Locate every malaria parasite.
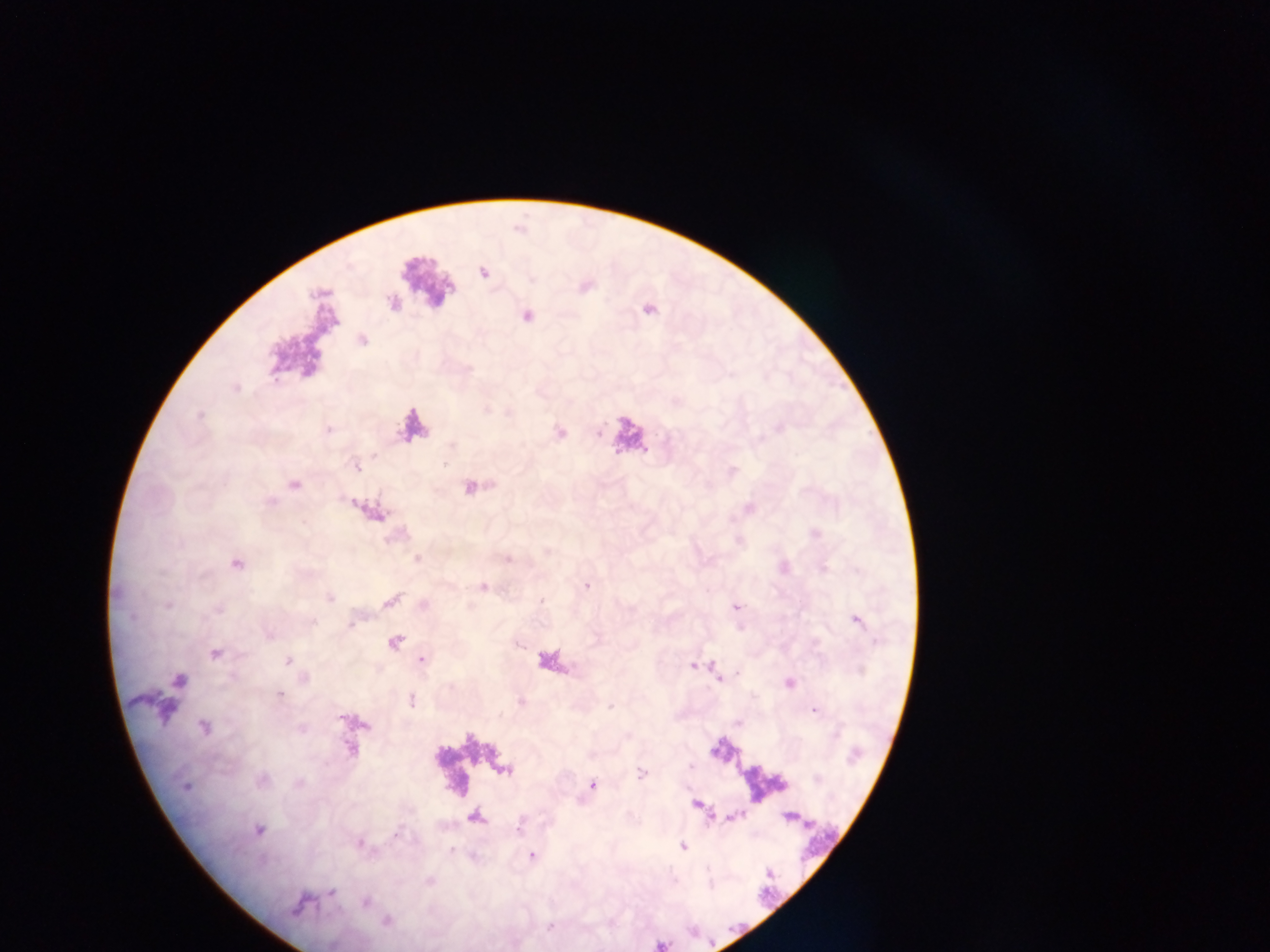
Approximate centers as x y in pixels.
Malaria parasites: 483 272; 647 308; 526 315; 362 339; 558 433; 357 467; 732 471; 294 485; 471 487; 371 511; 815 534; 507 558; 417 559; 235 563; 783 566; 586 585; 483 587; 329 597; 390 600; 423 605; 735 606; 856 620; 394 642; 215 653; 421 659; 287 661; 694 665; 717 678; 178 681; 789 682; 279 694; 410 700; 814 708; 203 727; 351 747; 641 772; 261 780; 592 784; 184 785; 695 804; 789 816; 474 818; 257 829; 683 846; 530 855; 331 892; 365 901; 299 903; 386 921.

Summary:
  - Leukocyte locations: 426 285; 412 425; 628 435
  - Field of view: single
  - Capture: mobile-phone photograph through a microscope
  - Image size: 1270×952 pixels
  - Country: Ghana
  - Preparation: thick blood smear